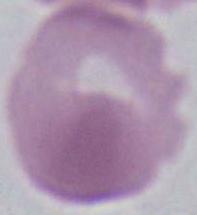
modality = micrograph
magnification = 1000x
identification = red blood cell